Assess for Plasmodium parasites.
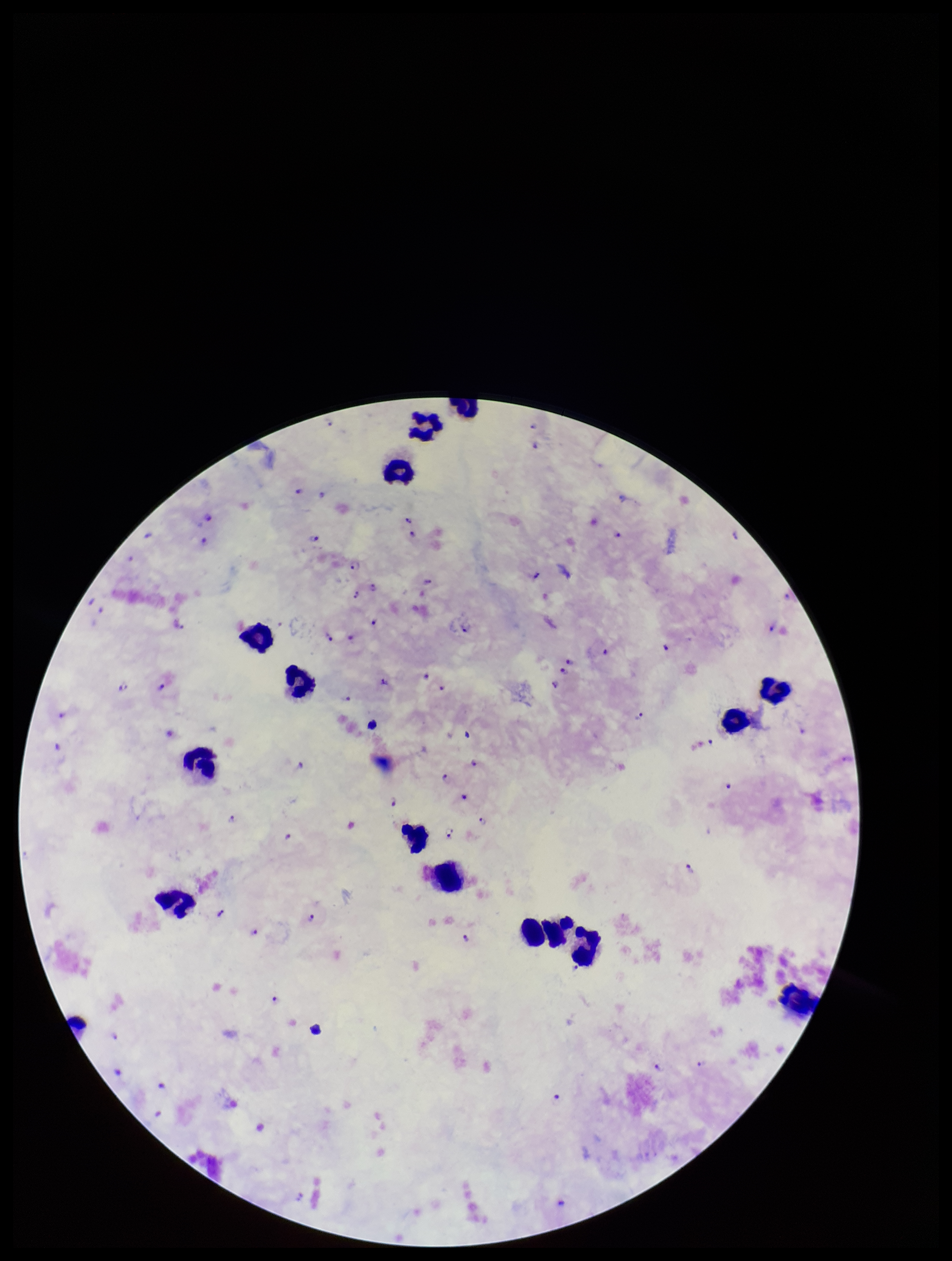

Detected.

Leukocyte count: 15. Parasite count: 80. Smartphone photograph taken through the eyepiece of a microscope. Image is 952×1261 pixels. One field from this slide. Preparation: thick smear. Giemsa stain. Patient malaria status: positive. Species reported for this patient: Plasmodium falciparum.